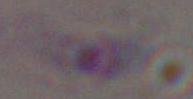
Toxoplasma gondii is seen. Photomicrograph. Captured at 1000x magnification.